Assess the morphology of the red blood cells.
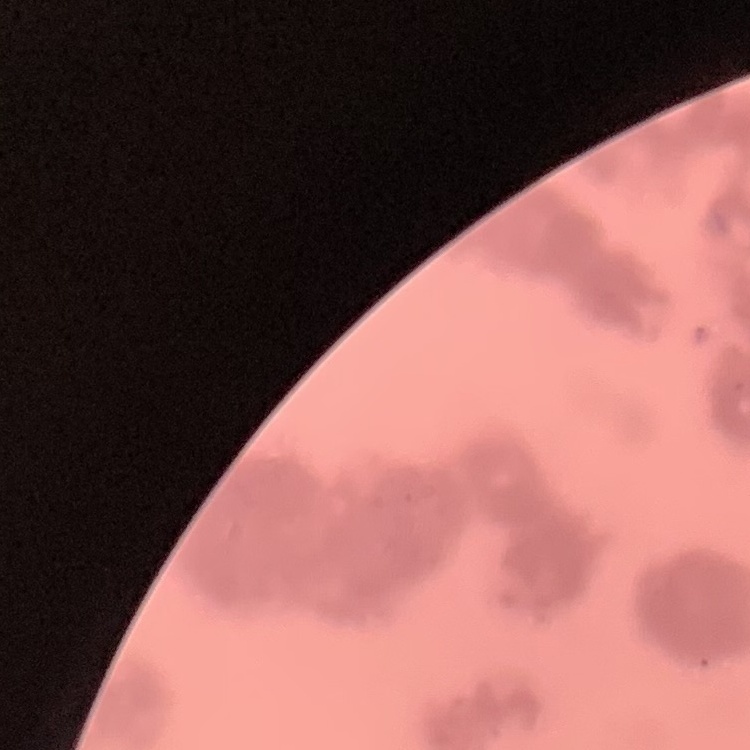
Rouleaux formation.

Summary:
  - Preparation: thin blood film
  - Image type: one tile cut from a larger photomicrograph
  - Stain: Field's or Giemsa